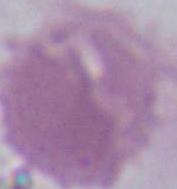
magnification = 1000x
identification = erythrocyte
modality = photomicrograph